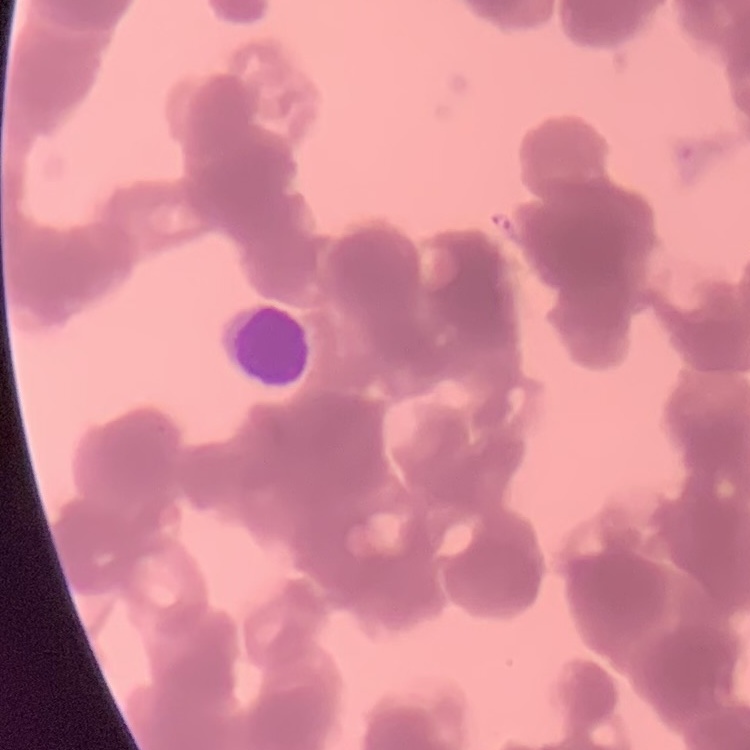 The erythrocytes exhibit rouleaux formation. Thin blood film. Square crop of a larger photomicrograph. Field's or Giemsa stain.